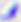
Summary:
  - Magnification: 400x
  - Identification: Toxoplasma gondii
  - Modality: micrograph